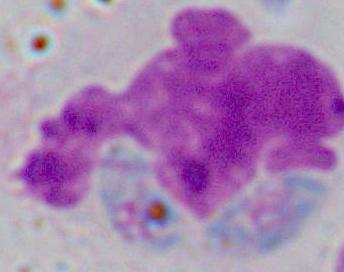

modality = photomicrograph
identification = white blood cell
magnification = 1000x